Identify the parasite.
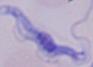
A trypanosome.

1000x magnification. Photomicrograph.